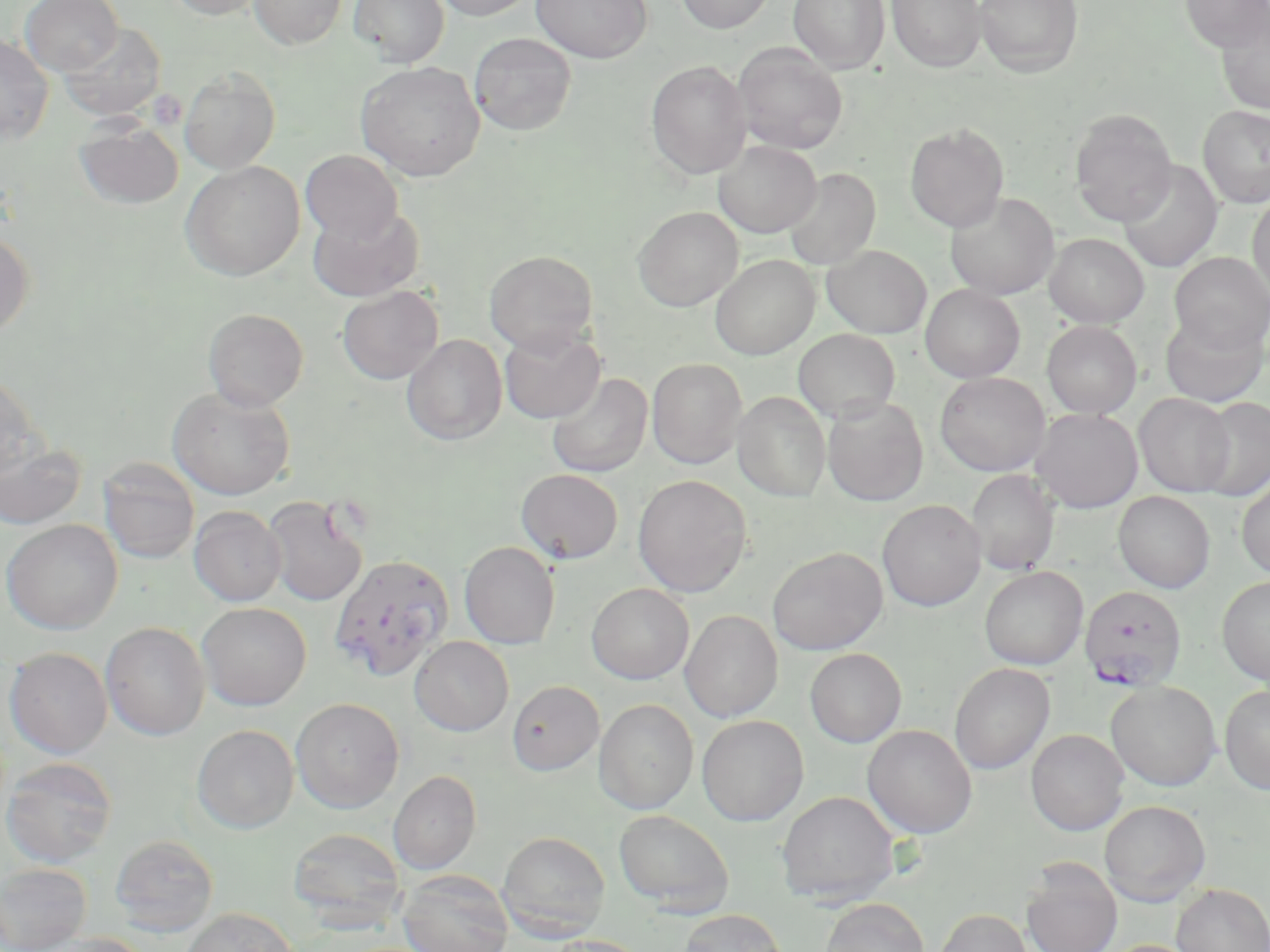 Approximate bounding boxes as named x1/y1/x2/y2 corners in pixels. Plasmodium falciparum-infected red blood cell locations (subset): (x1=1079, y1=585, x2=1188, y2=691). Platelet locations: (x1=147, y1=90, x2=187, y2=129). Uninfected red blood cell locations (subset): (x1=20, y1=0, x2=123, y2=75), (x1=165, y1=0, x2=268, y2=20), (x1=249, y1=0, x2=347, y2=49), (x1=348, y1=0, x2=449, y2=66), (x1=432, y1=0, x2=538, y2=20), (x1=532, y1=0, x2=652, y2=63), (x1=674, y1=0, x2=775, y2=34), (x1=788, y1=0, x2=890, y2=74), (x1=887, y1=0, x2=987, y2=73), (x1=974, y1=0, x2=1083, y2=78), (x1=1179, y1=0, x2=1269, y2=52), (x1=1217, y1=12, x2=1270, y2=115), (x1=58, y1=22, x2=166, y2=121), (x1=469, y1=31, x2=576, y2=135), (x1=0, y1=33, x2=54, y2=144), (x1=732, y1=43, x2=848, y2=154), (x1=645, y1=60, x2=751, y2=179), (x1=355, y1=61, x2=485, y2=181), (x1=179, y1=67, x2=280, y2=174), (x1=1198, y1=105, x2=1270, y2=208), (x1=1069, y1=108, x2=1177, y2=226), (x1=75, y1=118, x2=183, y2=209), (x1=905, y1=123, x2=1009, y2=232), (x1=713, y1=140, x2=821, y2=238), (x1=300, y1=150, x2=403, y2=243), (x1=180, y1=160, x2=305, y2=280), (x1=1118, y1=160, x2=1223, y2=273), (x1=783, y1=168, x2=880, y2=271), (x1=945, y1=192, x2=1059, y2=300), (x1=1248, y1=193, x2=1270, y2=301), (x1=309, y1=204, x2=425, y2=302), (x1=633, y1=206, x2=743, y2=311), (x1=0, y1=231, x2=35, y2=339), (x1=1044, y1=233, x2=1149, y2=327), (x1=821, y1=244, x2=932, y2=338), (x1=484, y1=251, x2=598, y2=355), (x1=1169, y1=252, x2=1269, y2=354), (x1=710, y1=255, x2=819, y2=359), (x1=921, y1=284, x2=1025, y2=382), (x1=337, y1=286, x2=443, y2=384), (x1=203, y1=308, x2=309, y2=410), (x1=1160, y1=310, x2=1269, y2=407), (x1=1042, y1=321, x2=1142, y2=418), (x1=500, y1=327, x2=605, y2=424), (x1=793, y1=328, x2=900, y2=423), (x1=402, y1=334, x2=507, y2=445), (x1=648, y1=358, x2=746, y2=468), (x1=0, y1=372, x2=45, y2=481), (x1=546, y1=372, x2=652, y2=478), (x1=935, y1=372, x2=1050, y2=476), (x1=167, y1=386, x2=295, y2=500), (x1=733, y1=391, x2=830, y2=502), (x1=1135, y1=393, x2=1235, y2=497), (x1=822, y1=396, x2=928, y2=506), (x1=1195, y1=397, x2=1270, y2=500), (x1=1031, y1=408, x2=1143, y2=513), (x1=0, y1=437, x2=86, y2=531), (x1=98, y1=458, x2=200, y2=564), (x1=516, y1=469, x2=623, y2=564), (x1=967, y1=470, x2=1059, y2=575), (x1=633, y1=474, x2=752, y2=597), (x1=1236, y1=475, x2=1270, y2=579), (x1=1113, y1=491, x2=1215, y2=593), (x1=263, y1=495, x2=369, y2=606), (x1=877, y1=499, x2=986, y2=611), (x1=189, y1=506, x2=286, y2=606), (x1=1, y1=519, x2=123, y2=634), (x1=459, y1=541, x2=560, y2=649), (x1=767, y1=547, x2=888, y2=655), (x1=979, y1=566, x2=1088, y2=669), (x1=1217, y1=576, x2=1270, y2=686), (x1=586, y1=583, x2=694, y2=684), (x1=196, y1=602, x2=312, y2=710), (x1=681, y1=610, x2=782, y2=722), (x1=100, y1=621, x2=210, y2=740), (x1=409, y1=636, x2=514, y2=736), (x1=4, y1=647, x2=112, y2=758), (x1=805, y1=648, x2=906, y2=747), (x1=949, y1=663, x2=1055, y2=774), (x1=507, y1=680, x2=604, y2=775), (x1=1105, y1=681, x2=1221, y2=791), (x1=1219, y1=685, x2=1270, y2=794), (x1=290, y1=698, x2=405, y2=813), (x1=594, y1=698, x2=699, y2=814), (x1=696, y1=714, x2=809, y2=826), (x1=192, y1=724, x2=299, y2=833), (x1=862, y1=724, x2=977, y2=838), (x1=1025, y1=728, x2=1129, y2=835), (x1=0, y1=756, x2=118, y2=867), (x1=388, y1=771, x2=481, y2=874), (x1=777, y1=790, x2=900, y2=906), (x1=1098, y1=800, x2=1210, y2=906), (x1=613, y1=809, x2=735, y2=915), (x1=287, y1=828, x2=406, y2=928), (x1=497, y1=831, x2=610, y2=941), (x1=109, y1=834, x2=219, y2=937), (x1=1021, y1=860, x2=1122, y2=952), (x1=0, y1=863, x2=92, y2=952), (x1=398, y1=870, x2=514, y2=952), (x1=1171, y1=884, x2=1269, y2=951), (x1=820, y1=898, x2=929, y2=952), (x1=179, y1=907, x2=297, y2=952), (x1=934, y1=908, x2=1033, y2=952), (x1=679, y1=909, x2=786, y2=952), (x1=39, y1=933, x2=155, y2=952), (x1=542, y1=935, x2=650, y2=952), (x1=1097, y1=939, x2=1202, y2=952). Slide-level diagnosis: Plasmodium falciparum. Thin blood smear. Light microscopy. Single field of view. 1000x magnification. Image is 1270×952 pixels. May-Grünwald-Giemsa stain.